Assess this cell for malaria.
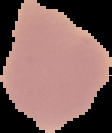
Uninfected.

Cell region segmented out of the field of view; the surrounding area is masked to black. From a thin blood smear. Image is 112×133 pixels.